Locate every Plasmodium vivax-infected red blood cell.
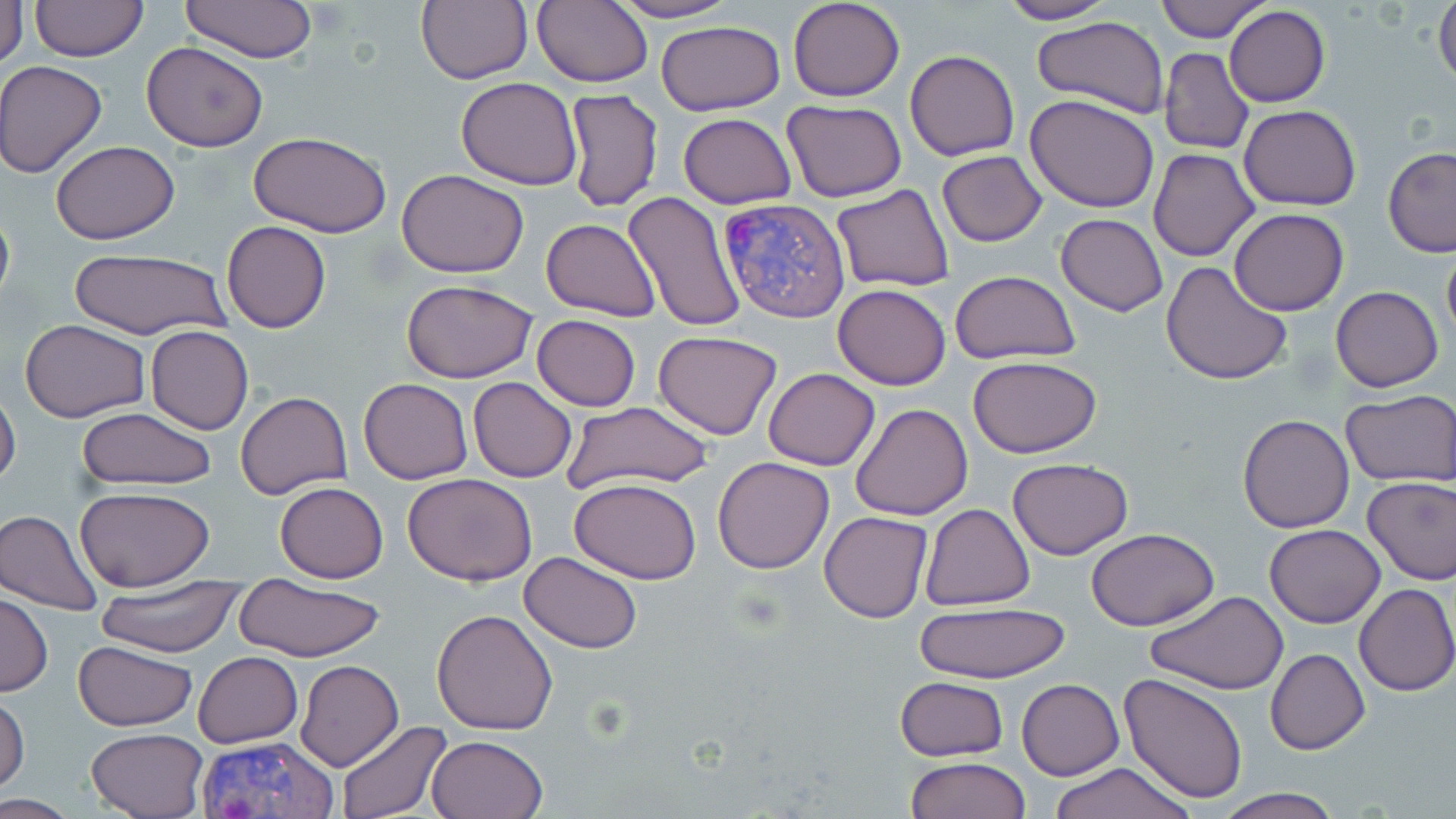

Approximate bounding boxes as (x1,y1)-(x2,y2) corner pairs in pixels.
Plasmodium vivax-infected red blood cells: (717,196)-(852,321), (196,737)-(338,819).

Uninfected red blood cell locations: (29,0)-(147,61), (179,0)-(317,65), (416,0)-(532,85), (532,0)-(653,87), (602,0)-(740,23), (787,0)-(906,102), (994,0)-(1119,24), (1153,0)-(1272,41), (1433,0)-(1456,92), (1,1)-(27,71), (1224,7)-(1330,107), (1030,16)-(1174,121), (656,21)-(787,116), (140,41)-(268,152), (1158,48)-(1253,155), (904,49)-(1021,162), (1,60)-(107,177), (456,76)-(583,189), (564,88)-(661,212), (1025,94)-(1159,212), (783,99)-(908,201), (1239,105)-(1361,211), (678,112)-(797,208), (248,132)-(392,239), (50,140)-(180,244), (1383,146)-(1456,256), (1149,148)-(1261,262), (936,150)-(1047,247), (396,170)-(529,276), (831,183)-(955,292), (621,191)-(747,331), (0,197)-(15,318), (1229,209)-(1349,315), (1055,213)-(1168,315), (542,217)-(660,321), (222,221)-(332,333), (1441,244)-(1456,351), (65,248)-(234,342), (1160,261)-(1294,387), (950,270)-(1080,364), (402,280)-(538,384), (832,283)-(950,390), (1331,286)-(1443,392), (531,314)-(641,412), (19,319)-(149,421), (145,325)-(254,434), (652,330)-(783,440), (967,356)-(1102,457), (764,368)-(880,470), (468,377)-(576,482), (359,378)-(473,485), (0,386)-(21,493), (236,392)-(352,499), (1341,392)-(1456,487), (560,400)-(713,492), (851,402)-(974,521), (75,407)-(219,490), (1237,414)-(1355,533), (712,456)-(835,574), (1008,457)-(1132,560), (404,473)-(538,586), (1361,474)-(1456,585), (571,478)-(701,583), (275,482)-(388,582), (75,486)-(214,592), (920,504)-(1035,610), (1,508)-(104,616), (820,511)-(933,623), (1264,524)-(1385,628), (1086,529)-(1218,630), (519,552)-(644,653), (89,576)-(247,656), (233,577)-(387,662), (1355,583)-(1456,696), (1145,590)-(1289,696), (0,592)-(54,696), (913,602)-(1072,682), (432,608)-(560,734), (71,640)-(198,731), (1266,648)-(1369,754), (193,650)-(303,747), (296,659)-(404,771), (1120,672)-(1248,803), (895,675)-(1009,762), (1017,679)-(1123,780), (0,693)-(28,796), (335,721)-(451,818), (86,728)-(208,818), (426,735)-(548,819), (907,757)-(1031,818), (1045,762)-(1197,819), (1207,789)-(1350,819), (0,795)-(86,816). Slide-level diagnosis: Plasmodium vivax. Thin blood smear. Optical microscopy. May-Grünwald-Giemsa-stained preparation. Image is 1456×819 pixels. One field of a larger specimen. 1000x magnification.